Classify this cell by malaria status.
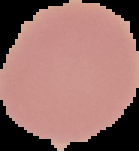
It is uninfected.

The area outside the segmented cell region is set to black. Image is 139×151 pixels. From a thin blood film.